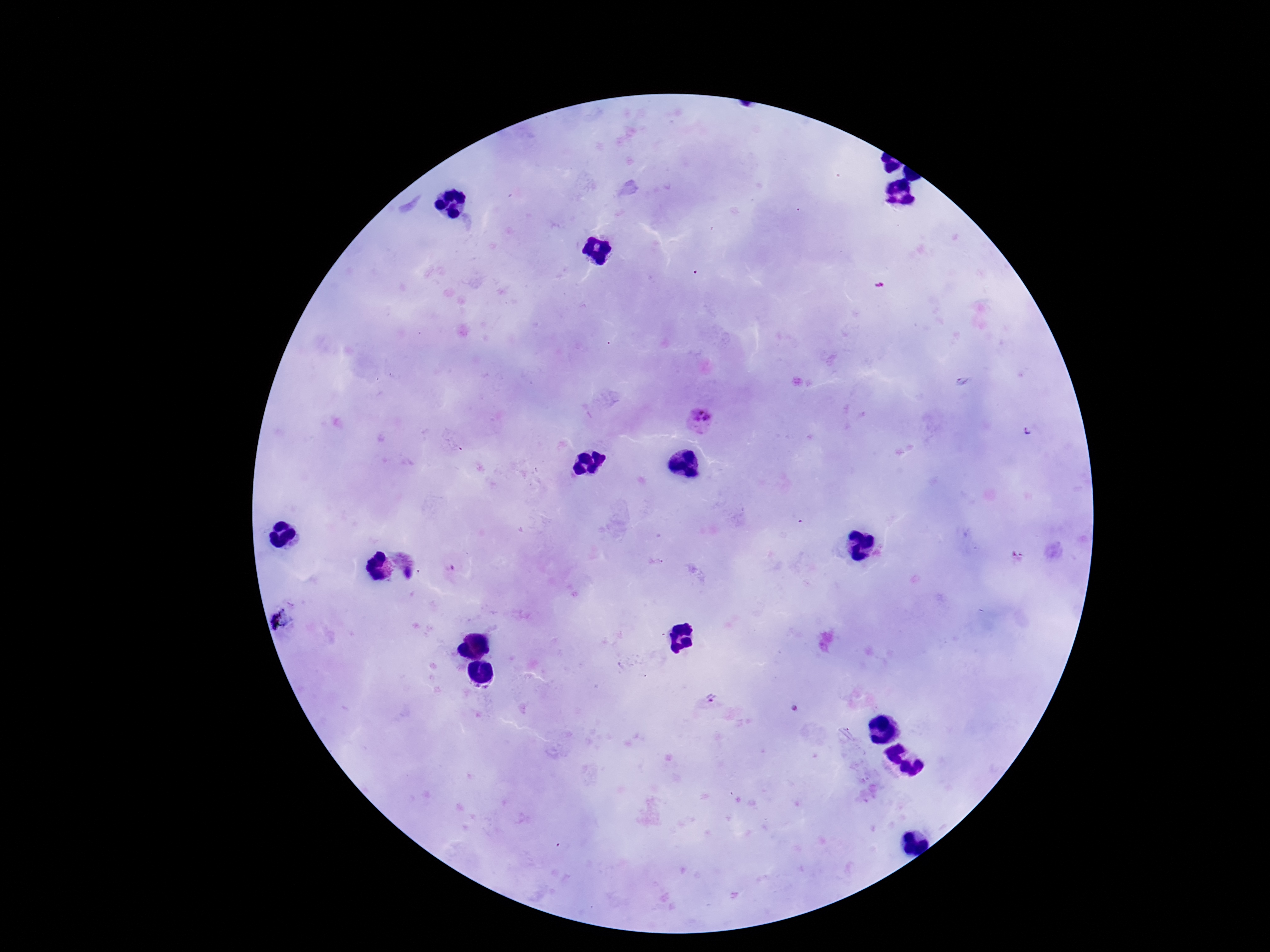

Approximate centers as {x, y} in pixels.
Summary:
  - Plasmodium parasite locations: {702, 419}, {408, 563}, {711, 697}
  - Magnification: 100x
  - Stain: Giemsa
  - Image size: 1270×952 pixels
  - Patient malaria status: positive
  - Preparation: thick peripheral-blood smear
  - Capture: smartphone camera through the microscope eyepiece
  - Field of view: one from this slide